State the preparation type.
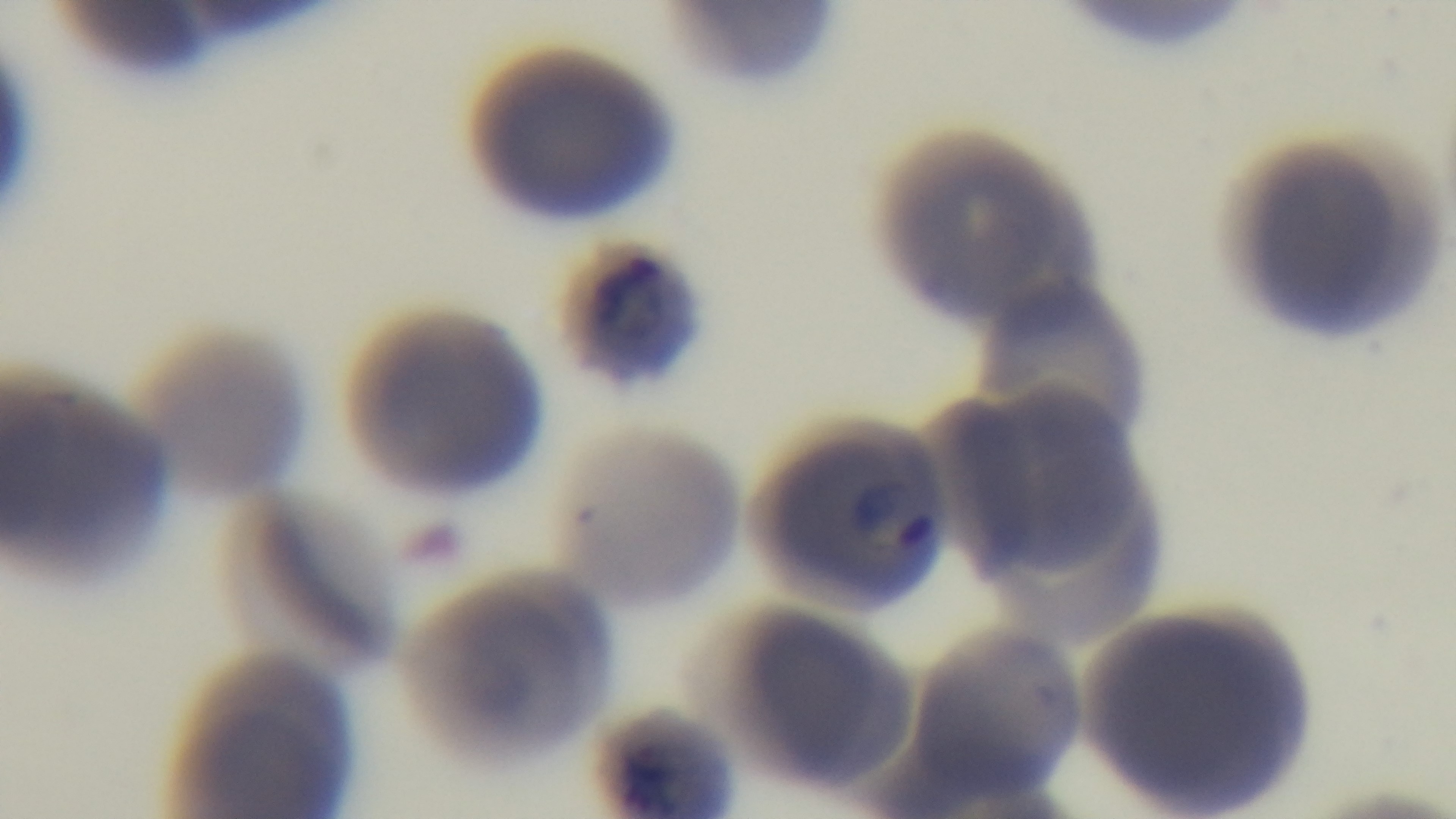
A thin smear.

Summary:
  - Objective: 100x oil immersion
  - Capture: mounted 4K digital camera
  - Modality: light microscopy
  - Stain: Giemsa
  - Field of view: one from the slide
  - Malaria status: infected